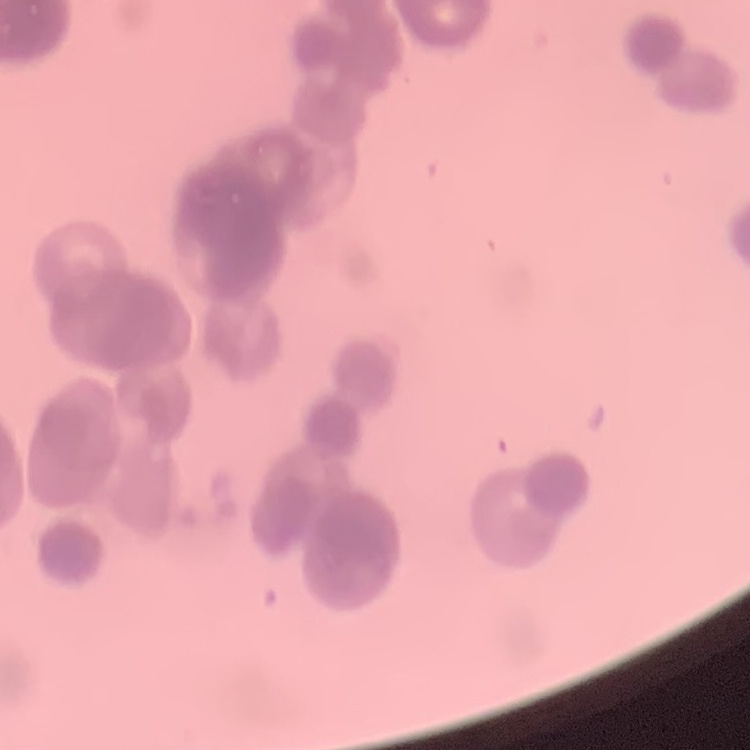
The red blood cells show rouleaux formation. Square crop of a larger photomicrograph. Thin blood smear. Stained with either Field's or Giemsa.